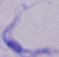
A trypanosome is seen. Photomicrograph. 1000x magnification.